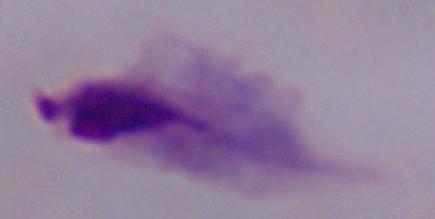 1000x magnification. A trichomonad is shown. Photomicrograph.